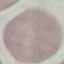
Summary:
  - Result: negative for malaria parasites
  - Stain: Giemsa
  - Capture: smartphone camera at the microscope eyepiece
  - Preparation: thin smear
  - Image type: cell patch, automatically extracted from a larger field of view and resized to 64 × 64 pixels